Report the malaria status of this cell.
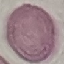

It is uninfected.

Summary:
  - Image type: automatically extracted cell patch, resized to 64 × 64 pixels
  - Preparation: thin blood smear
  - Stain: Giemsa
  - Capture: smartphone camera at the microscope eyepiece